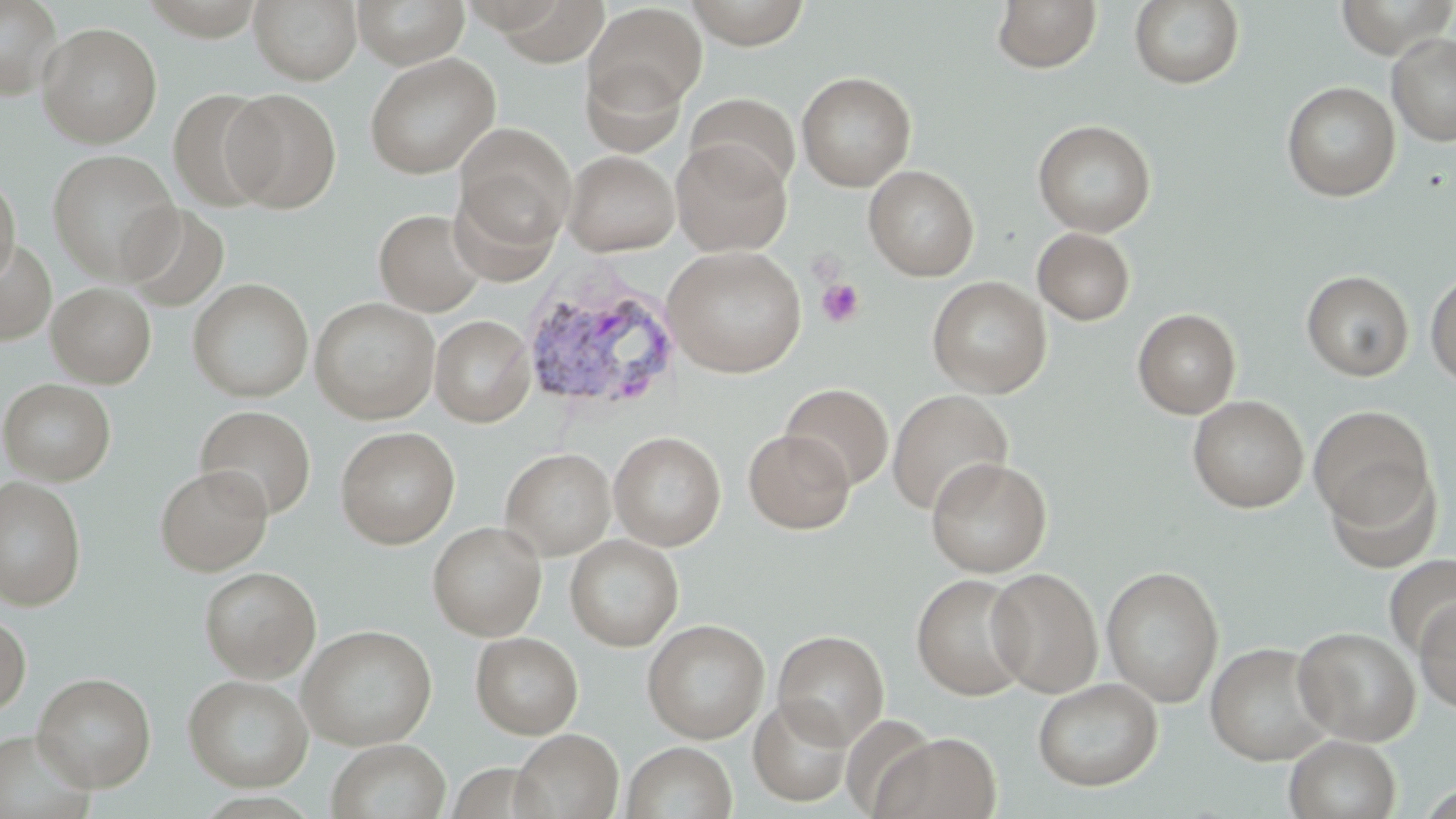
{
  "slide_level_diagnosis": "Plasmodium vivax",
  "magnification": "1000x",
  "preparation": "thin blood film",
  "image_size": "1456×819 pixels",
  "field_of_view": "one of a larger specimen",
  "modality": "optical microscopy",
  "plasmodium_vivax_infected_red_blood_cell_locations": "approximate bounding boxes as (x1, y1, x2, y2) in pixels: (518, 269, 683, 416)",
  "uninfected_red_blood_cell_locations": "approximate bounding boxes as (x1, y1, x2, y2) in pixels: (0, 0, 64, 100), (249, 0, 362, 84), (353, 0, 470, 68), (682, 0, 813, 48), (992, 0, 1101, 73), (1129, 0, 1245, 89), (1334, 0, 1456, 58), (584, 3, 707, 114), (37, 22, 162, 147), (1387, 32, 1456, 146), (363, 52, 501, 179), (579, 58, 686, 158), (796, 71, 917, 191), (1282, 81, 1401, 201), (222, 88, 342, 213), (169, 89, 281, 211), (685, 93, 800, 196), (1032, 119, 1156, 237), (451, 133, 574, 265), (671, 139, 792, 256), (46, 149, 181, 282), (563, 150, 680, 255), (864, 165, 979, 280), (0, 170, 20, 289), (120, 203, 229, 311), (374, 208, 487, 316), (1032, 227, 1136, 326), (0, 239, 57, 346), (662, 245, 808, 378), (1301, 270, 1414, 381), (1425, 270, 1456, 389), (927, 276, 1052, 397), (188, 278, 313, 403), (47, 283, 156, 387), (310, 297, 440, 423), (1133, 308, 1241, 418), (430, 315, 536, 427), (1, 378, 116, 486), (781, 383, 894, 491), (887, 389, 1014, 516), (1187, 395, 1309, 513), (194, 405, 316, 520), (1308, 405, 1434, 527), (335, 426, 460, 549), (743, 429, 854, 533), (609, 430, 726, 550), (501, 448, 616, 560), (926, 456, 1052, 577), (1324, 461, 1441, 571), (155, 465, 272, 576), (0, 476, 87, 610), (428, 521, 546, 640), (565, 534, 684, 651), (1384, 554, 1456, 659), (1101, 565, 1224, 707), (199, 566, 321, 682), (986, 568, 1103, 696), (911, 573, 1033, 700), (1415, 598, 1456, 712), (0, 612, 31, 716), (642, 619, 770, 743), (297, 624, 437, 750), (1293, 626, 1421, 745), (773, 629, 890, 748), (471, 632, 583, 739), (1205, 642, 1334, 764), (32, 672, 156, 791), (183, 674, 313, 791), (1032, 677, 1163, 792), (748, 696, 854, 806), (511, 728, 624, 819), (0, 730, 95, 819), (874, 731, 1001, 819), (1284, 734, 1401, 819), (327, 739, 451, 819), (622, 741, 737, 819)",
  "platelet_locations": "approximate bounding boxes as (x1, y1, x2, y2) in pixels: (817, 278, 864, 328)",
  "stain": "May-Grünwald-Giemsa"
}